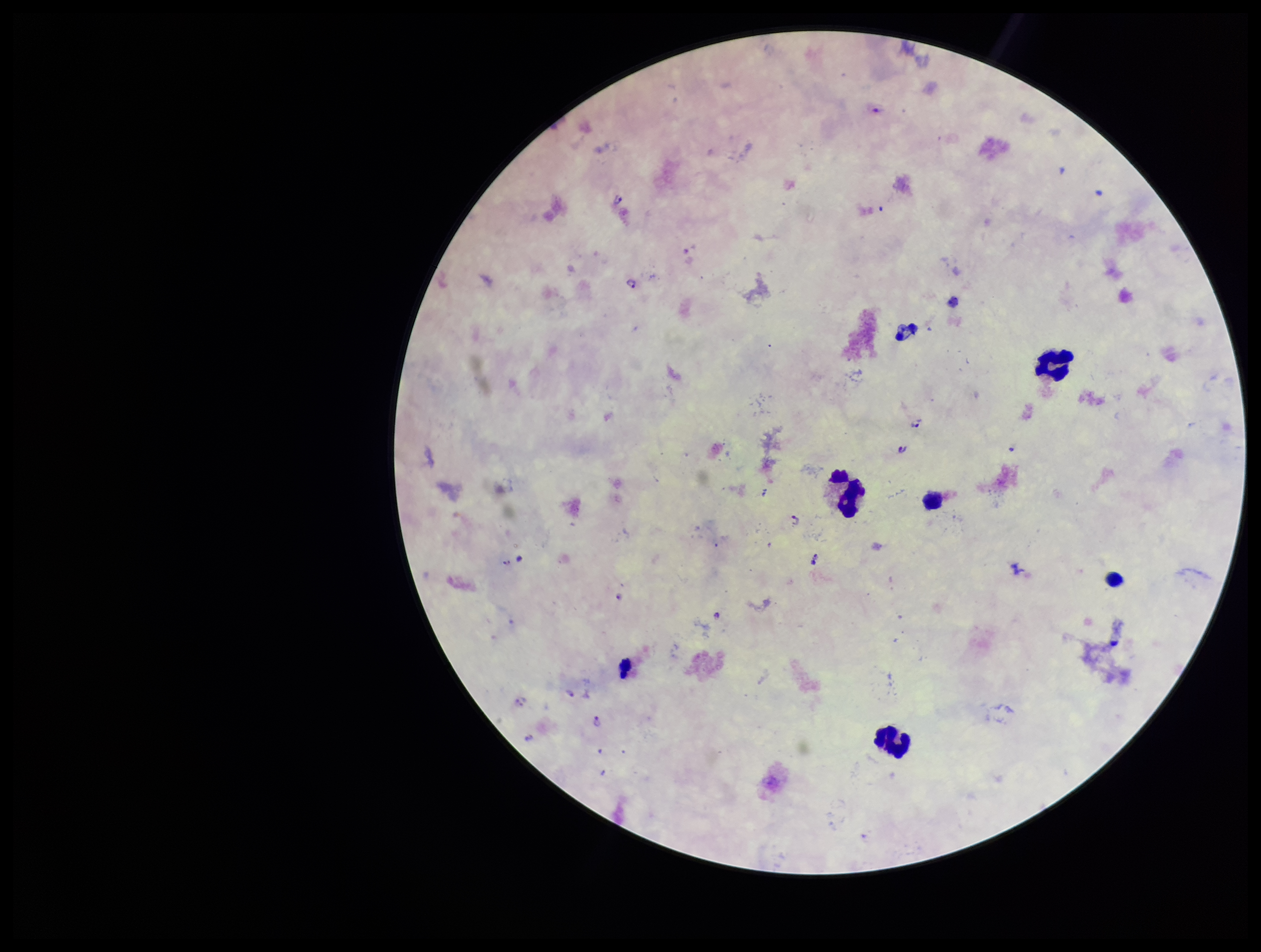 Patient malaria status: positive. Plasmodium parasites: detected. Image is 1261×952 pixels. Parasite count: 9. Preparation: thick. Single field of view. Photographed through the microscope eyepiece with a smartphone camera. Stained with Giemsa. Species reported for this patient: Plasmodium falciparum. Leukocyte count: 5.